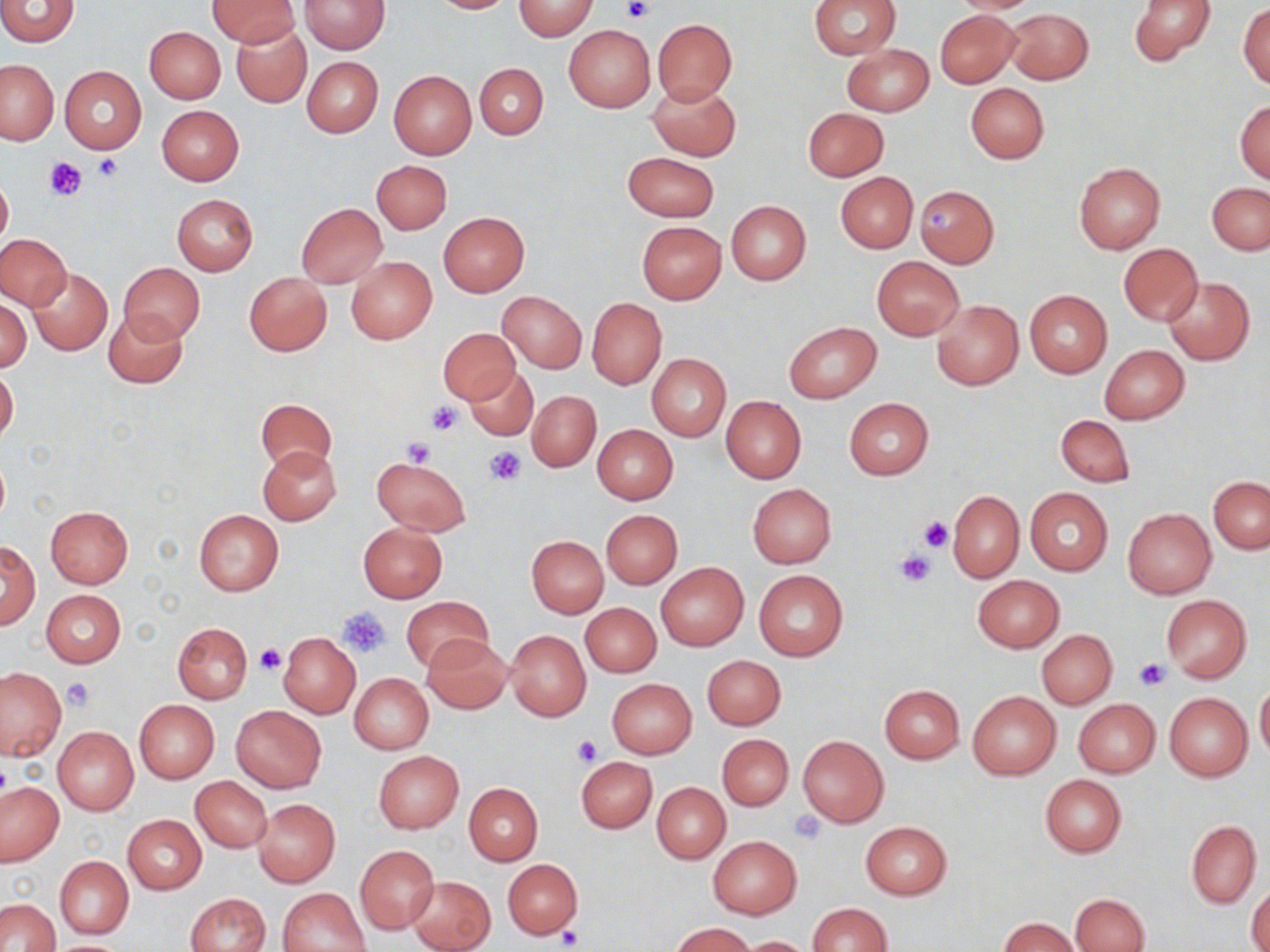
Approximate bounding boxes as named x1/y1/x2/y2 corners in pixels. Uninfected red blood cell locations: (x1=205, y1=0, x2=300, y2=47), (x1=426, y1=0, x2=517, y2=14), (x1=809, y1=0, x2=900, y2=59), (x1=944, y1=0, x2=1047, y2=14), (x1=1129, y1=0, x2=1217, y2=67), (x1=0, y1=1, x2=80, y2=47), (x1=299, y1=1, x2=389, y2=54), (x1=513, y1=1, x2=598, y2=40), (x1=1238, y1=3, x2=1269, y2=90), (x1=1004, y1=7, x2=1093, y2=84), (x1=935, y1=9, x2=1022, y2=88), (x1=652, y1=18, x2=736, y2=104), (x1=231, y1=21, x2=311, y2=107), (x1=563, y1=24, x2=656, y2=112), (x1=144, y1=26, x2=225, y2=104), (x1=842, y1=43, x2=934, y2=116), (x1=303, y1=56, x2=382, y2=136), (x1=0, y1=58, x2=59, y2=146), (x1=475, y1=62, x2=548, y2=139), (x1=60, y1=66, x2=147, y2=155), (x1=389, y1=70, x2=476, y2=159), (x1=648, y1=82, x2=741, y2=160), (x1=965, y1=83, x2=1050, y2=164), (x1=1235, y1=99, x2=1270, y2=184), (x1=156, y1=105, x2=245, y2=185), (x1=802, y1=107, x2=889, y2=181), (x1=622, y1=152, x2=718, y2=222), (x1=371, y1=160, x2=452, y2=234), (x1=1073, y1=162, x2=1165, y2=254), (x1=835, y1=171, x2=918, y2=254), (x1=0, y1=172, x2=13, y2=253), (x1=1207, y1=182, x2=1269, y2=254), (x1=914, y1=185, x2=999, y2=268), (x1=172, y1=194, x2=258, y2=275), (x1=725, y1=200, x2=810, y2=286), (x1=296, y1=203, x2=388, y2=288), (x1=437, y1=211, x2=529, y2=297), (x1=636, y1=220, x2=726, y2=304), (x1=1, y1=233, x2=72, y2=310), (x1=1119, y1=244, x2=1204, y2=325), (x1=346, y1=256, x2=438, y2=344), (x1=872, y1=256, x2=963, y2=340), (x1=120, y1=262, x2=205, y2=342), (x1=28, y1=268, x2=112, y2=355), (x1=244, y1=272, x2=332, y2=356), (x1=1164, y1=276, x2=1254, y2=365), (x1=1025, y1=289, x2=1112, y2=377), (x1=498, y1=290, x2=586, y2=373), (x1=1, y1=296, x2=31, y2=374), (x1=587, y1=297, x2=666, y2=390), (x1=931, y1=299, x2=1024, y2=391), (x1=104, y1=308, x2=188, y2=388), (x1=783, y1=321, x2=882, y2=404), (x1=439, y1=328, x2=519, y2=404), (x1=1100, y1=345, x2=1189, y2=425), (x1=646, y1=354, x2=730, y2=442), (x1=0, y1=367, x2=19, y2=445), (x1=466, y1=367, x2=538, y2=440), (x1=528, y1=390, x2=600, y2=471), (x1=721, y1=396, x2=806, y2=484), (x1=843, y1=397, x2=934, y2=480), (x1=256, y1=398, x2=336, y2=475), (x1=1055, y1=413, x2=1135, y2=487), (x1=593, y1=425, x2=678, y2=505), (x1=257, y1=446, x2=342, y2=525), (x1=372, y1=456, x2=471, y2=536), (x1=1208, y1=476, x2=1269, y2=554), (x1=748, y1=485, x2=836, y2=567), (x1=1024, y1=487, x2=1113, y2=576), (x1=949, y1=491, x2=1024, y2=581), (x1=45, y1=505, x2=133, y2=587), (x1=1123, y1=508, x2=1217, y2=599), (x1=194, y1=509, x2=284, y2=595), (x1=600, y1=509, x2=682, y2=589), (x1=358, y1=522, x2=447, y2=602), (x1=527, y1=536, x2=608, y2=617), (x1=0, y1=540, x2=38, y2=629), (x1=655, y1=562, x2=748, y2=651), (x1=754, y1=571, x2=848, y2=661), (x1=974, y1=575, x2=1063, y2=652), (x1=40, y1=589, x2=125, y2=668), (x1=1162, y1=594, x2=1251, y2=683), (x1=402, y1=596, x2=492, y2=672), (x1=581, y1=602, x2=661, y2=676), (x1=172, y1=622, x2=252, y2=703), (x1=505, y1=629, x2=591, y2=722), (x1=1037, y1=631, x2=1117, y2=708), (x1=279, y1=632, x2=360, y2=719), (x1=422, y1=633, x2=512, y2=713), (x1=702, y1=655, x2=786, y2=729), (x1=0, y1=668, x2=65, y2=759), (x1=349, y1=673, x2=433, y2=754), (x1=606, y1=678, x2=696, y2=758), (x1=1255, y1=682, x2=1270, y2=761), (x1=878, y1=684, x2=965, y2=763), (x1=968, y1=691, x2=1061, y2=779), (x1=1165, y1=691, x2=1252, y2=781), (x1=1072, y1=698, x2=1160, y2=777), (x1=135, y1=700, x2=219, y2=783), (x1=232, y1=705, x2=327, y2=792), (x1=53, y1=726, x2=139, y2=816), (x1=718, y1=734, x2=794, y2=810), (x1=798, y1=735, x2=888, y2=827), (x1=374, y1=751, x2=462, y2=833), (x1=576, y1=756, x2=657, y2=832), (x1=1039, y1=774, x2=1127, y2=857), (x1=191, y1=776, x2=272, y2=852), (x1=0, y1=782, x2=63, y2=865), (x1=652, y1=782, x2=730, y2=863), (x1=464, y1=784, x2=542, y2=864), (x1=253, y1=798, x2=340, y2=887), (x1=123, y1=814, x2=206, y2=894), (x1=1186, y1=820, x2=1261, y2=907), (x1=860, y1=821, x2=952, y2=899), (x1=708, y1=836, x2=802, y2=918), (x1=355, y1=845, x2=439, y2=933), (x1=54, y1=856, x2=133, y2=939), (x1=502, y1=859, x2=583, y2=939), (x1=407, y1=875, x2=494, y2=951), (x1=1247, y1=881, x2=1270, y2=952), (x1=278, y1=887, x2=370, y2=952), (x1=184, y1=892, x2=270, y2=952), (x1=1069, y1=893, x2=1150, y2=952), (x1=0, y1=899, x2=59, y2=952), (x1=806, y1=903, x2=893, y2=951), (x1=1001, y1=918, x2=1079, y2=951), (x1=672, y1=922, x2=754, y2=952), (x1=739, y1=935, x2=814, y2=951), (x1=44, y1=939, x2=134, y2=952). Platelet locations: (x1=621, y1=0, x2=654, y2=24), (x1=93, y1=154, x2=124, y2=182), (x1=43, y1=158, x2=85, y2=204), (x1=927, y1=204, x2=953, y2=230), (x1=427, y1=400, x2=461, y2=434), (x1=402, y1=438, x2=434, y2=467), (x1=484, y1=447, x2=525, y2=486), (x1=918, y1=517, x2=953, y2=552), (x1=895, y1=549, x2=935, y2=587), (x1=338, y1=605, x2=390, y2=658), (x1=254, y1=645, x2=284, y2=675), (x1=1135, y1=658, x2=1171, y2=691), (x1=62, y1=678, x2=94, y2=710), (x1=570, y1=734, x2=602, y2=765), (x1=788, y1=808, x2=826, y2=843), (x1=556, y1=926, x2=583, y2=949). Slide-level diagnosis: no evidence of blood parasites. May-Grünwald-Giemsa stain. Image is 1270×952 pixels. Single field of view. Light microscopy. Thin blood smear. Captured at 1000x magnification.